Draw a bounding box around every Plasmodium parasite, every leukocyte, and every artifact (stain precipitate or debris).
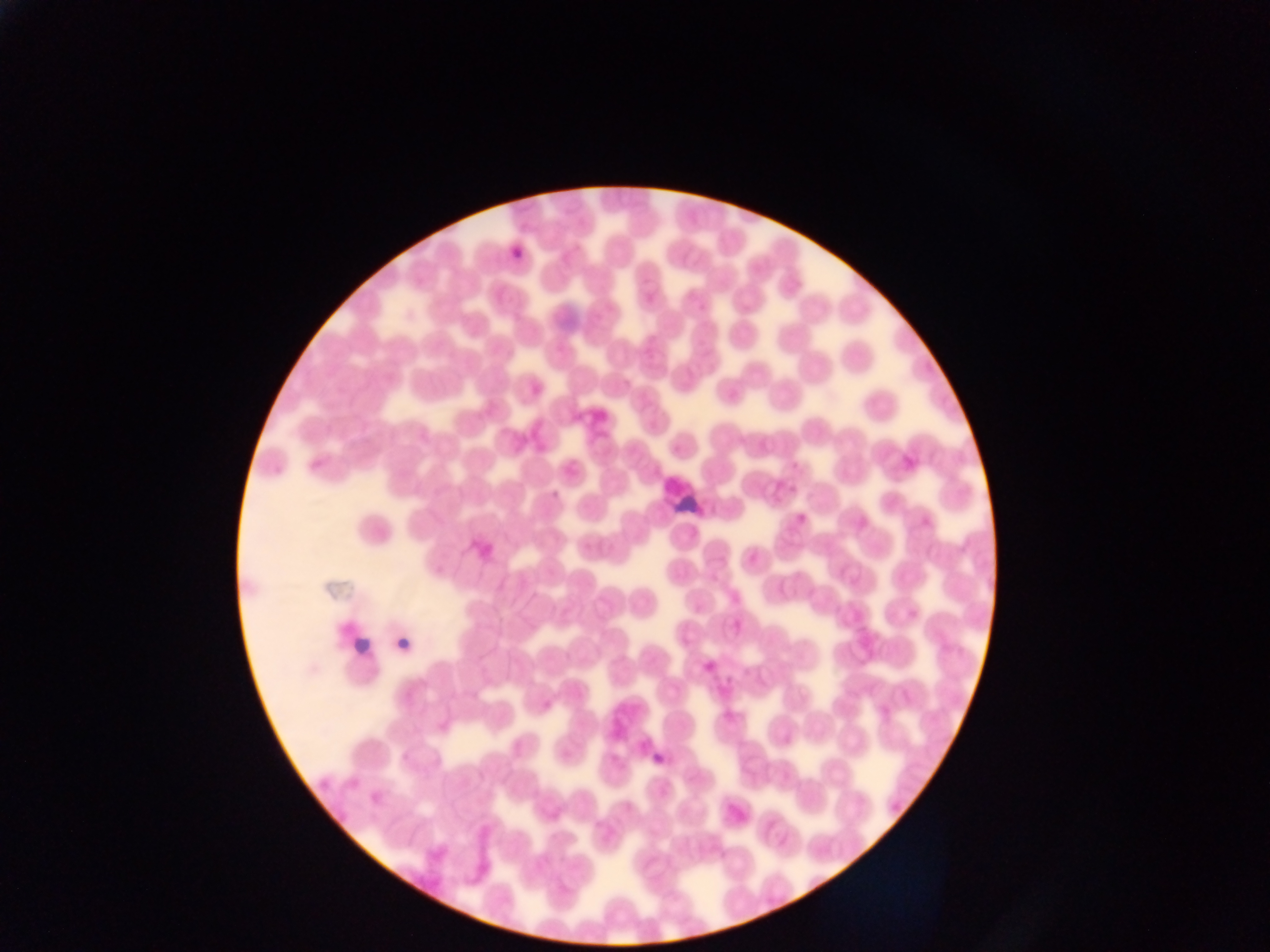
Approximate bounding boxes as (left, top, right, bottom) in pixels.
Plasmodium parasites: (510, 245, 527, 258), (549, 485, 563, 500), (792, 508, 809, 523), (721, 707, 733, 727), (652, 746, 669, 770).
Leukocytes: (343, 625, 375, 659).
Artifacts (stain precipitate or debris): (655, 472, 721, 530).

One field of view. Mobile-phone photograph taken through the microscope. Image is 1270×952 pixels. Thin blood film. Sample from Ghana.